Assess this cell for malaria.
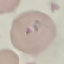

Parasitized.

{
  "stain": "Giemsa",
  "preparation": "thin blood film",
  "capture": "smartphone camera at the microscope eyepiece",
  "image_type": "cell patch, automatically extracted from a larger field of view and resized to 64 × 64 pixels"
}